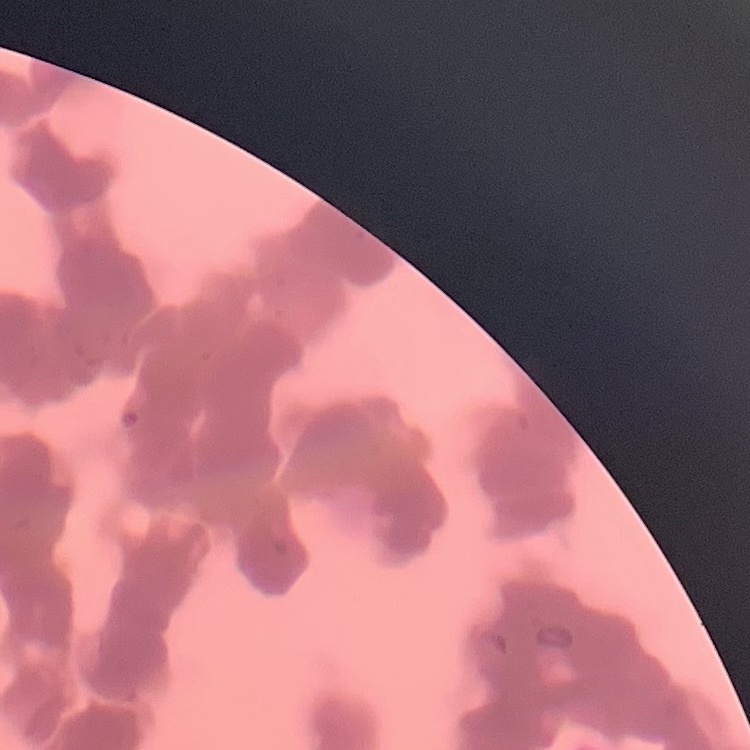

{
  "red_blood_cell_morphology": "rouleaux formation",
  "preparation": "thin peripheral smear",
  "image_type": "one tile cut from a larger photomicrograph",
  "stain": "Field's or Giemsa"
}